Assess this cell for malaria.
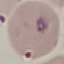
Parasitized.

Cell patch, automatically extracted from a larger field of view and resized to 64 × 64 pixels. Thin blood smear. Acquired by smartphone through the microscope eyepiece. Giemsa stain.